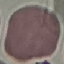
Summary:
  - Malaria status: uninfected
  - Preparation: thin blood smear
  - Image type: cell patch, automatically extracted from a larger field of view and resized to 64 × 64 pixels
  - Stain: Giemsa
  - Capture: smartphone camera at the microscope eyepiece